Identify the blood parasite species.
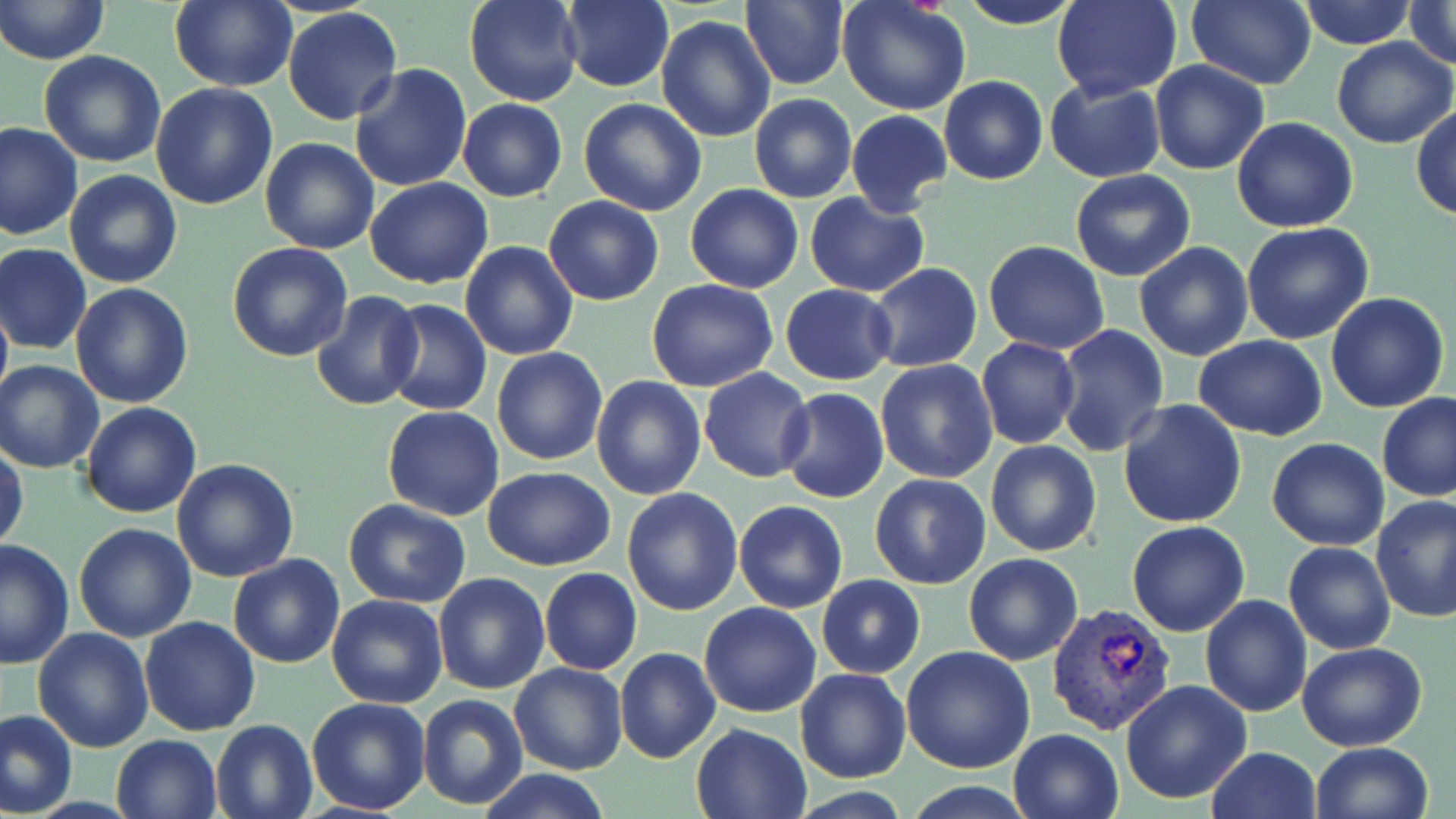
Plasmodium vivax.

{
  "stain": "May-Grünwald-Giemsa",
  "modality": "light microscopy",
  "plasmodium_vivax_infected_red_blood_cell_locations": "approximate bounding boxes as (x1, y1, x2, y2) in pixels: (1046, 603, 1178, 737)",
  "magnification": "1000x",
  "field_of_view": "one of a larger specimen",
  "uninfected_red_blood_cell_locations": "approximate bounding boxes as (x1, y1, x2, y2) in pixels: (0, 0, 112, 67), (464, 0, 582, 106), (740, 0, 850, 91), (958, 0, 1084, 28), (1052, 0, 1183, 100), (1187, 0, 1315, 90), (1299, 0, 1416, 50), (1404, 0, 1455, 70), (168, 1, 298, 90), (556, 1, 674, 92), (837, 1, 971, 115), (282, 7, 403, 125), (656, 15, 775, 142), (1330, 36, 1454, 149), (38, 51, 167, 168), (1150, 60, 1269, 175), (350, 65, 472, 193), (938, 76, 1049, 186), (1044, 80, 1165, 183), (149, 83, 278, 210), (749, 94, 858, 203), (458, 98, 567, 202), (578, 98, 707, 218), (1413, 105, 1456, 223), (845, 110, 952, 215), (1231, 115, 1359, 234), (0, 122, 82, 241), (261, 138, 380, 255), (1069, 168, 1196, 282), (65, 169, 182, 288), (366, 178, 494, 289), (685, 184, 803, 293), (804, 192, 929, 295), (543, 196, 666, 307), (1241, 223, 1374, 344), (984, 239, 1110, 354), (459, 241, 579, 362), (226, 242, 353, 363), (1134, 242, 1254, 363), (1, 244, 93, 355), (868, 262, 983, 374), (339, 265, 464, 430), (646, 278, 778, 392), (70, 282, 195, 408), (781, 284, 896, 384), (310, 290, 423, 410), (1325, 291, 1450, 412), (0, 293, 11, 414), (384, 300, 491, 416), (1053, 324, 1169, 458), (1194, 335, 1327, 439), (976, 339, 1080, 450), (490, 346, 608, 466), (0, 360, 105, 472), (875, 360, 997, 483), (700, 367, 815, 483), (592, 375, 706, 499), (29, 377, 174, 504), (777, 388, 888, 504), (1378, 393, 1456, 503), (1119, 400, 1247, 529), (81, 402, 201, 518), (383, 406, 504, 520), (1267, 438, 1390, 550), (985, 440, 1103, 556), (0, 442, 27, 554), (172, 457, 299, 582), (483, 465, 615, 571), (870, 474, 991, 590), (622, 487, 743, 615), (1372, 496, 1456, 624), (344, 498, 471, 606), (734, 500, 848, 614), (1127, 520, 1251, 637), (73, 522, 196, 642), (0, 540, 75, 669), (1283, 542, 1395, 655), (963, 553, 1084, 666), (227, 554, 346, 669), (539, 568, 641, 675), (432, 573, 551, 694), (816, 574, 925, 677), (326, 594, 450, 709), (1201, 594, 1312, 716), (698, 602, 821, 718), (138, 616, 262, 736), (642, 623, 795, 745), (33, 627, 157, 752), (1297, 642, 1426, 751), (902, 644, 1036, 774), (615, 647, 720, 764), (509, 662, 629, 776), (794, 667, 911, 783), (1120, 679, 1253, 804), (417, 694, 528, 810), (306, 697, 431, 816), (1, 707, 77, 816), (209, 718, 320, 819), (689, 722, 811, 818), (1007, 728, 1125, 819), (111, 734, 221, 818), (1310, 742, 1434, 819), (1205, 747, 1321, 819), (475, 767, 613, 819)",
  "image_size": "1456×819 pixels",
  "preparation": "thin blood film"
}